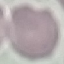
{
  "malaria_status": "uninfected",
  "stain": "Giemsa",
  "image_type": "cell patch, automatically extracted from a larger field of view and resized to 64 × 64 pixels",
  "capture": "smartphone through the microscope eyepiece",
  "preparation": "thin blood smear"
}